Assess this cell for malaria.
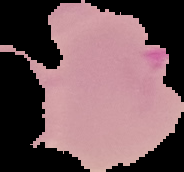
It is parasitized.

Cell region segmented out of the field of view; the surrounding area is masked to black. Image is 184×172 pixels. From a thin blood film.